Look for parasitized red blood cells.
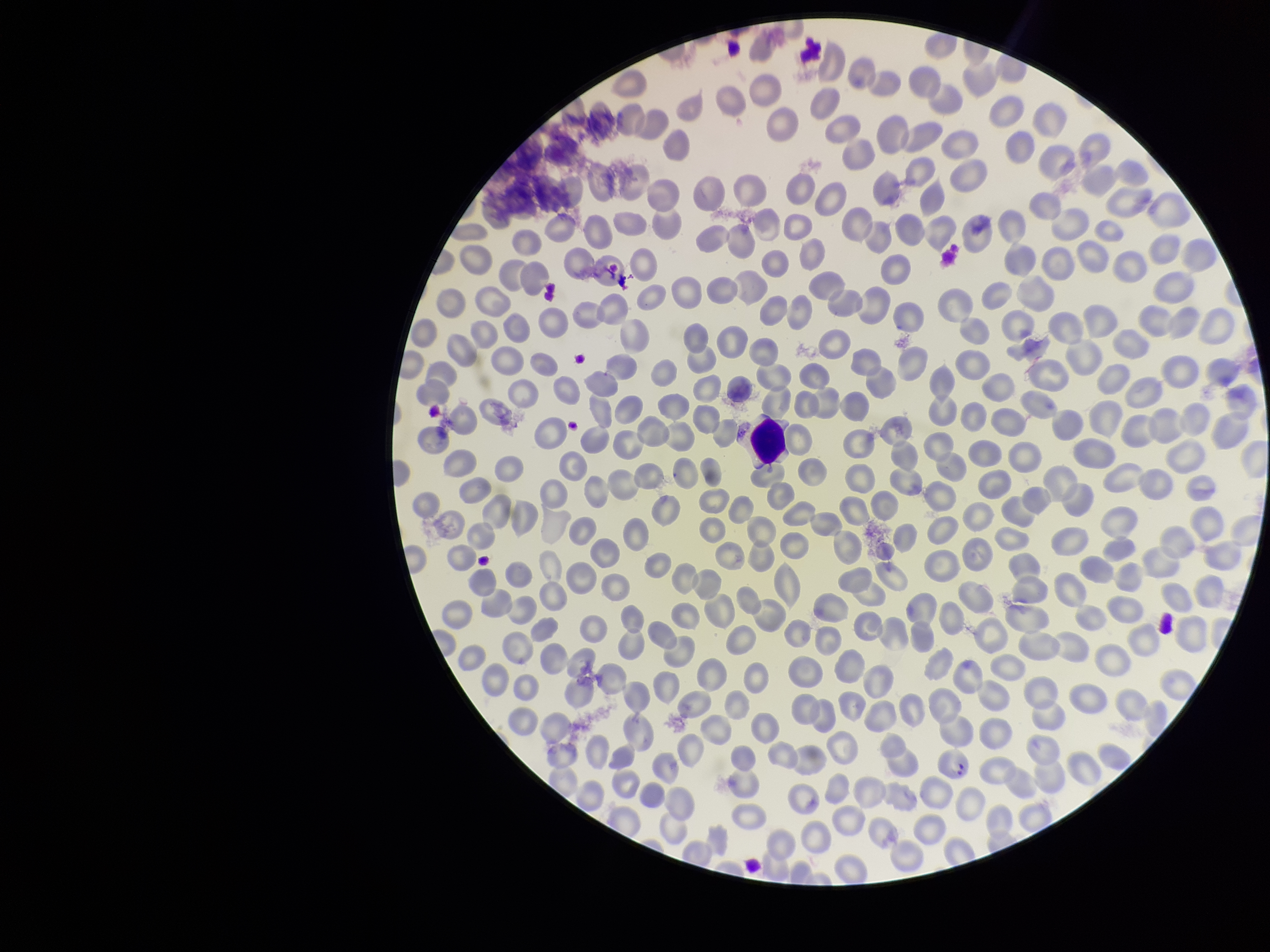

Detected.

{
  "image_size": "1270×952 pixels",
  "field_of_view": "single",
  "capture": "smartphone photograph through the microscope eyepiece",
  "preparation": "thin",
  "parasitized_red_blood_cell_count": 1,
  "red_blood_cell_count": 312,
  "patient_malaria_status": "infected",
  "species_reported_for_this_patient": "Plasmodium falciparum",
  "stain": "Giemsa"
}